Locate every Plasmodium falciparum-infected red blood cell.
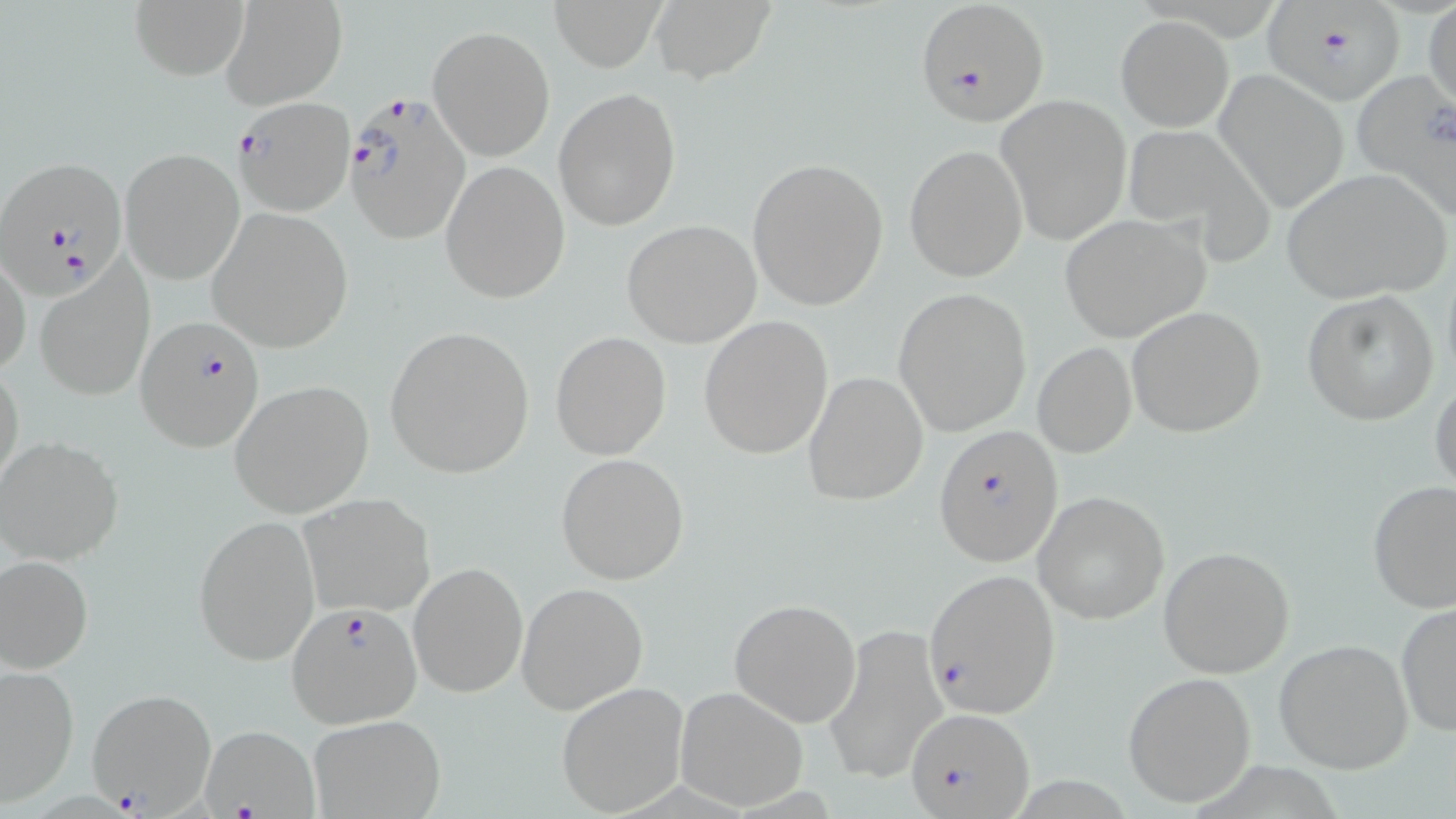
Approximate bounding boxes as named x1/y1/x2/y2 corners in pixels.
Plasmodium falciparum-infected red blood cells: (x1=914, y1=0, x2=1050, y2=128), (x1=1264, y1=4, x2=1404, y2=107), (x1=346, y1=92, x2=476, y2=249), (x1=232, y1=96, x2=355, y2=217), (x1=0, y1=154, x2=130, y2=297), (x1=135, y1=316, x2=265, y2=455), (x1=934, y1=425, x2=1063, y2=569), (x1=923, y1=568, x2=1061, y2=718), (x1=286, y1=602, x2=424, y2=728), (x1=86, y1=687, x2=218, y2=816), (x1=906, y1=705, x2=1035, y2=819), (x1=198, y1=727, x2=318, y2=817).

Summary:
  - Uninfected red blood cell locations: (x1=131, y1=0, x2=250, y2=81), (x1=219, y1=0, x2=348, y2=109), (x1=548, y1=0, x2=665, y2=69), (x1=1424, y1=0, x2=1456, y2=117), (x1=649, y1=1, x2=772, y2=82), (x1=1116, y1=15, x2=1232, y2=131), (x1=428, y1=25, x2=555, y2=160), (x1=1213, y1=69, x2=1349, y2=213), (x1=1350, y1=70, x2=1456, y2=216), (x1=553, y1=88, x2=680, y2=232), (x1=995, y1=93, x2=1133, y2=245), (x1=1120, y1=124, x2=1272, y2=256), (x1=904, y1=144, x2=1028, y2=281), (x1=121, y1=147, x2=245, y2=285), (x1=747, y1=158, x2=888, y2=310), (x1=439, y1=161, x2=569, y2=304), (x1=1278, y1=169, x2=1451, y2=306), (x1=207, y1=209, x2=353, y2=351), (x1=1058, y1=214, x2=1211, y2=342), (x1=621, y1=220, x2=762, y2=346), (x1=0, y1=254, x2=29, y2=379), (x1=35, y1=261, x2=156, y2=402), (x1=894, y1=287, x2=1032, y2=437), (x1=1302, y1=290, x2=1440, y2=425), (x1=1125, y1=305, x2=1267, y2=439), (x1=698, y1=316, x2=834, y2=459), (x1=384, y1=324, x2=536, y2=479), (x1=552, y1=332, x2=671, y2=459), (x1=1032, y1=343, x2=1137, y2=458), (x1=0, y1=360, x2=24, y2=494), (x1=803, y1=371, x2=929, y2=506), (x1=1429, y1=376, x2=1456, y2=499), (x1=230, y1=380, x2=374, y2=517), (x1=0, y1=436, x2=124, y2=565), (x1=555, y1=453, x2=689, y2=585), (x1=1367, y1=480, x2=1456, y2=612), (x1=1033, y1=491, x2=1170, y2=625), (x1=298, y1=493, x2=436, y2=618), (x1=194, y1=514, x2=320, y2=666), (x1=1156, y1=545, x2=1296, y2=679), (x1=0, y1=554, x2=93, y2=673), (x1=408, y1=561, x2=528, y2=700), (x1=516, y1=581, x2=649, y2=715), (x1=729, y1=596, x2=861, y2=726), (x1=1395, y1=601, x2=1456, y2=738), (x1=823, y1=624, x2=947, y2=786), (x1=1273, y1=638, x2=1414, y2=775), (x1=0, y1=665, x2=79, y2=806), (x1=1122, y1=672, x2=1258, y2=808), (x1=556, y1=681, x2=690, y2=817), (x1=674, y1=685, x2=809, y2=810), (x1=308, y1=713, x2=445, y2=819)
  - Slide-level diagnosis: Plasmodium falciparum
  - Stain: May-Grünwald-Giemsa
  - Field of view: single
  - Modality: optical microscopy
  - Image size: 1456×819 pixels
  - Preparation: thin blood film
  - Magnification: 1000x